Describe the morphology of the red blood cells.
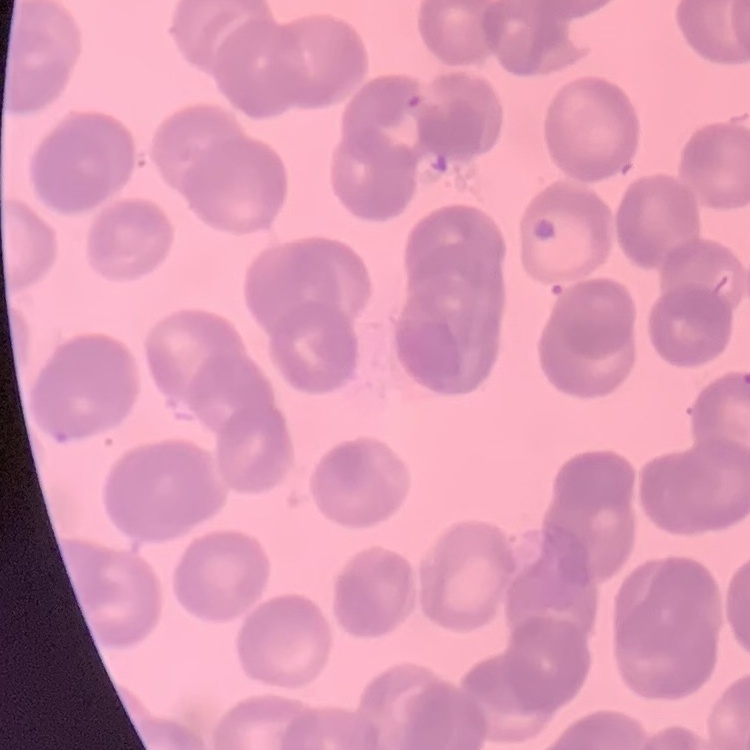

They show rouleaux formation.

One tile cut from a larger photomicrograph. Stained with either Field's or Giemsa. Thin peripheral smear.